Outline each blood parasite and name the species.
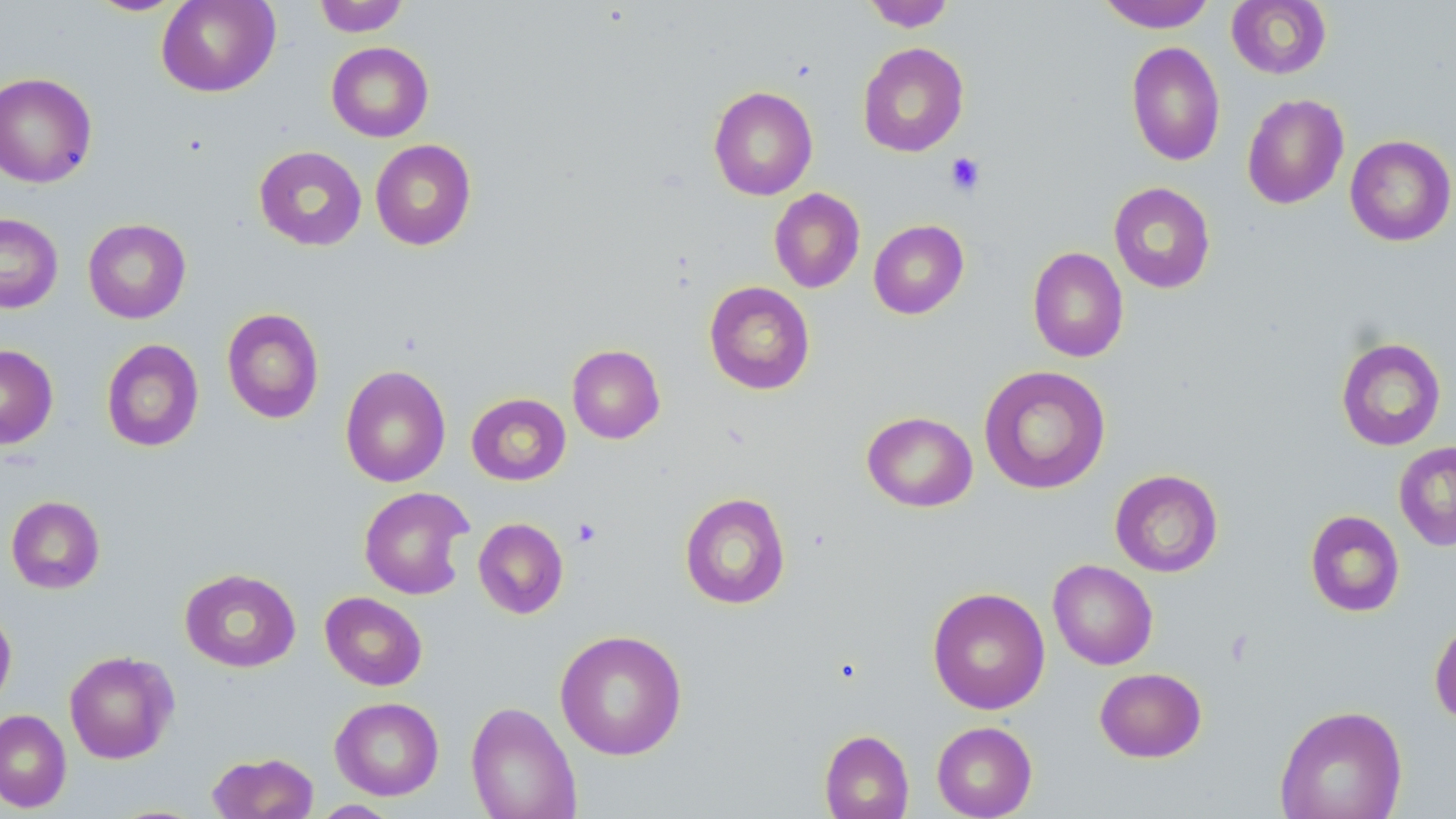
No blood parasites seen.

slide-level diagnosis = no evidence of blood parasites
preparation = thin blood film
stain = May-Grünwald-Giemsa
magnification = 1000x
platelet locations = approximate bounding boxes as [x1, y1, x2, y2] in pixels: [945, 152, 985, 197], [573, 518, 602, 547]
modality = optical microscopy
uninfected red blood cell locations = approximate bounding boxes as [x1, y1, x2, y2] in pixels: [156, 0, 281, 97], [313, 0, 409, 36], [861, 0, 955, 32], [1097, 0, 1217, 32], [1226, 0, 1332, 79], [84, 1, 188, 17], [1125, 41, 1225, 166], [326, 42, 434, 142], [857, 42, 969, 157], [0, 72, 97, 188], [709, 85, 818, 200], [1242, 93, 1349, 209], [1344, 134, 1456, 246], [370, 139, 476, 251], [253, 146, 367, 251], [1108, 182, 1216, 294], [769, 188, 865, 293], [0, 213, 62, 314], [83, 219, 191, 323], [868, 219, 969, 319], [1027, 246, 1129, 362], [704, 281, 816, 395], [222, 308, 324, 424], [1335, 337, 1446, 451], [101, 339, 204, 452], [0, 344, 58, 449], [567, 344, 665, 444], [339, 365, 451, 488], [978, 365, 1111, 495], [466, 393, 571, 486], [862, 411, 978, 512], [1393, 441, 1456, 551], [1110, 469, 1223, 577], [359, 486, 474, 600], [680, 492, 790, 609], [6, 495, 105, 594], [1304, 510, 1405, 617], [473, 517, 568, 619], [1047, 559, 1158, 670], [179, 568, 301, 672], [927, 587, 1050, 715], [320, 591, 428, 690], [0, 607, 17, 709], [1429, 617, 1456, 726], [554, 629, 688, 761], [64, 650, 179, 764], [1094, 667, 1207, 762], [330, 696, 445, 800], [465, 701, 581, 819], [1274, 704, 1407, 819], [0, 709, 71, 812], [931, 721, 1037, 818], [819, 729, 914, 819], [208, 752, 318, 819], [311, 800, 401, 818]
image size = 1456×819 pixels
field of view = single